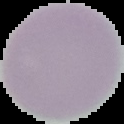 Result: no malaria parasites seen. Segmented cell region on a black background. From a thin blood smear. Image is 124×124 pixels.